Locate every Plasmodium parasite.
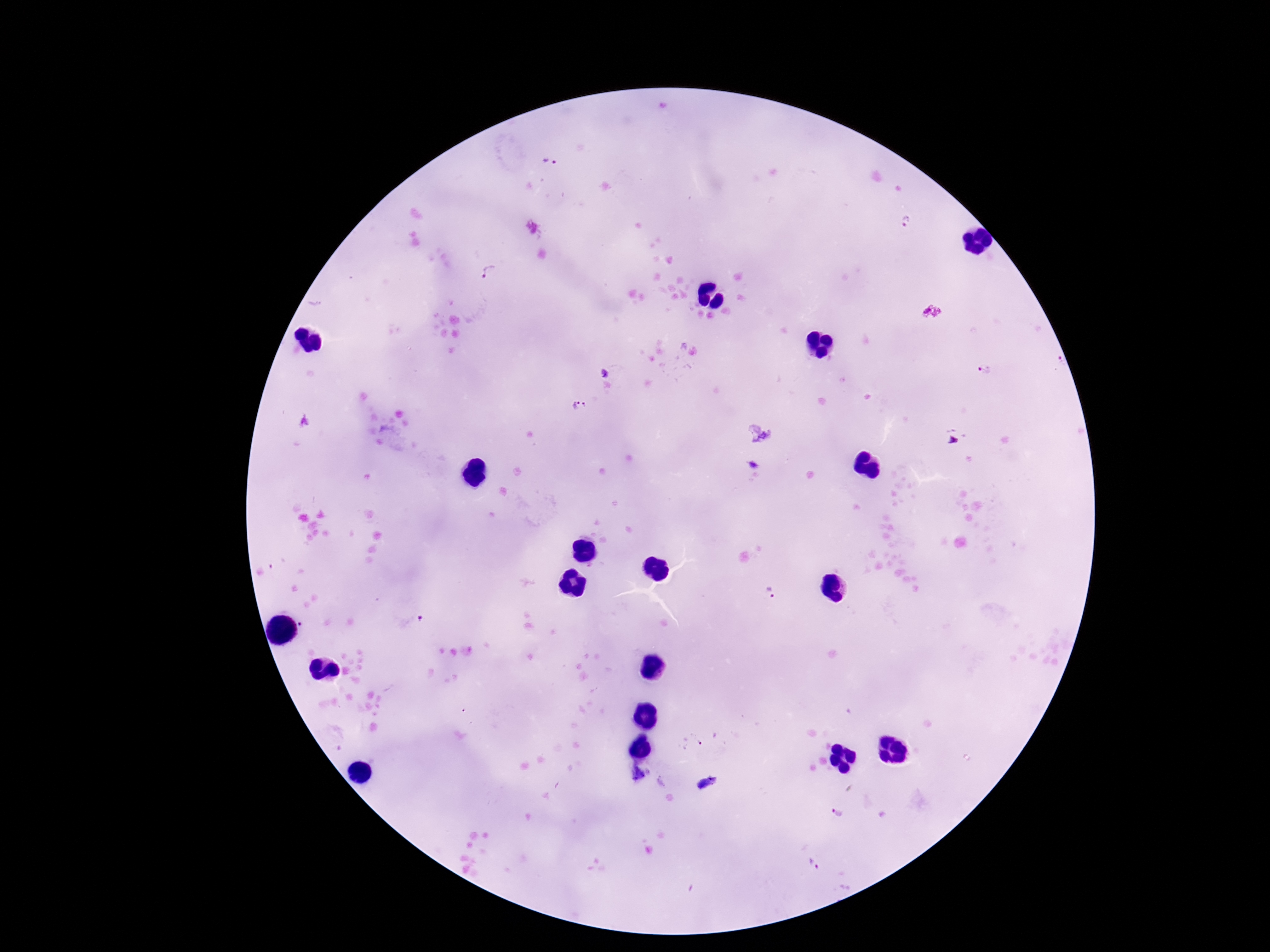

Approximate centers as [x, y] in pixels.
Plasmodium parasites: [552, 161], [906, 221], [490, 273], [604, 371], [983, 371], [581, 406], [769, 593], [410, 624], [693, 742], [837, 812].

image size = 1270×952 pixels
patient malaria status = infected
stain = Giemsa
magnification = 100x
field of view = single
capture = smartphone camera through the microscope eyepiece
preparation = thick blood film